Report the malaria status of this cell.
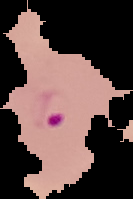
Parasitized.

Cell region segmented out of the field of view; the surrounding area is masked to black. From a thin blood film. Image is 133×199 pixels.